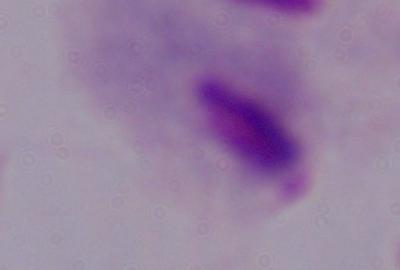 A trichomonad is shown. Photomicrograph. Captured at 1000x magnification.